Classify this cell by malaria status.
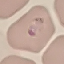
It is parasitized.

Giemsa-stained preparation. Automatically extracted cell patch, resized to 64 × 64 pixels. Thin blood film. Acquired by smartphone through the microscope eyepiece.